Point out each leukocyte.
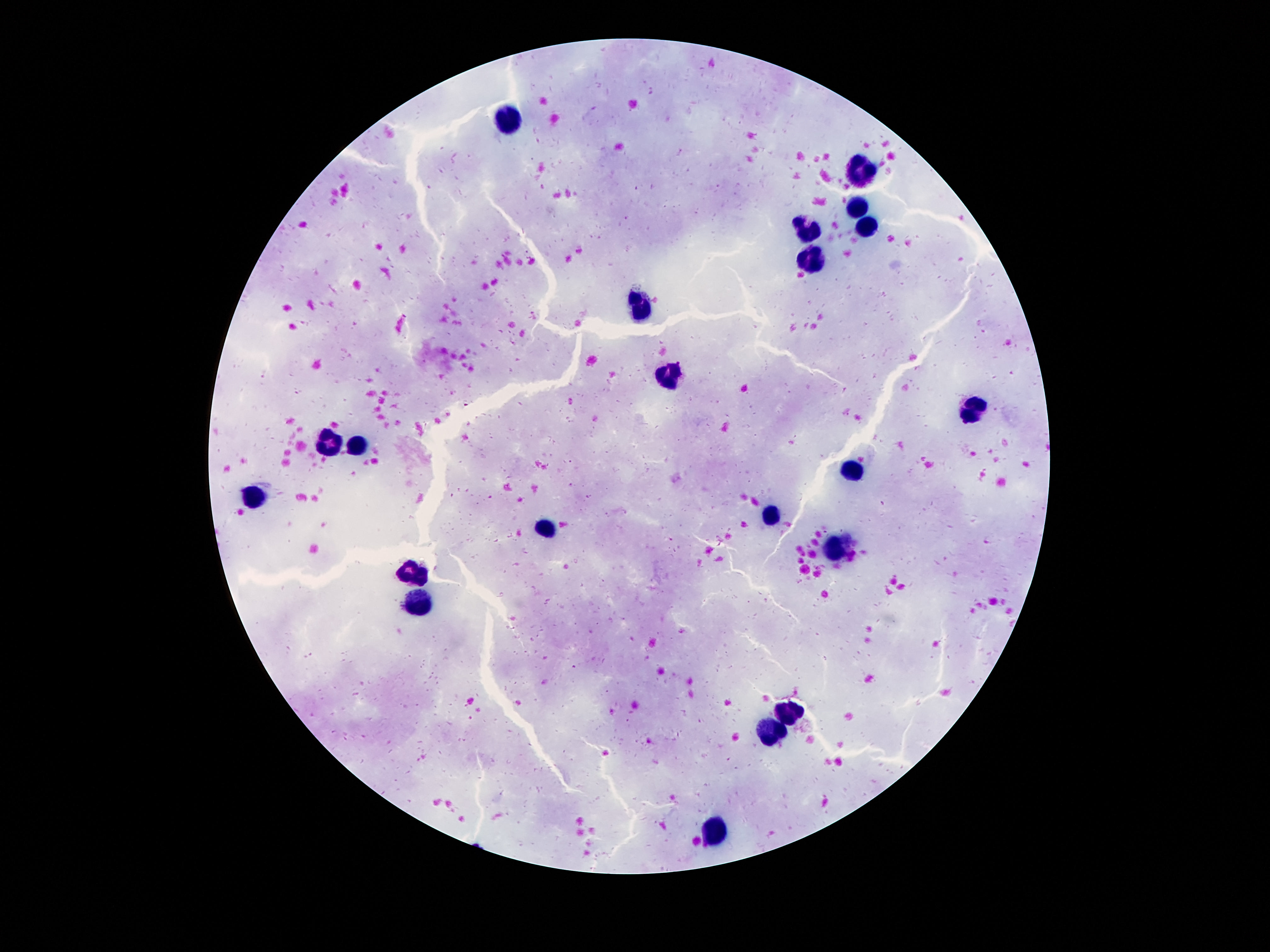
Approximate object centers, in pixels from the top-left corner.
Leukocytes: (x=505, y=119), (x=861, y=170), (x=859, y=207), (x=870, y=224), (x=809, y=229), (x=813, y=256), (x=639, y=304), (x=668, y=374), (x=972, y=408), (x=327, y=442), (x=359, y=446), (x=849, y=471), (x=250, y=496), (x=772, y=515), (x=545, y=530), (x=834, y=547), (x=421, y=574), (x=420, y=601), (x=790, y=708), (x=775, y=729), (x=715, y=831).

Image is 1270×952 pixels. Smartphone photograph taken through the microscope eyepiece. Patient malaria status: uninfected. Single field of view. Thick blood film. 100x magnification. Giemsa-stained preparation.